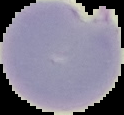

preparation: thin blood smear
result: malaria parasites detected
image_type: segmented cell region on a black background
image_size: 124×115 pixels